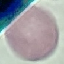
Summary:
  - Malaria status: uninfected
  - Image type: automatically extracted cell patch, resized to 64 × 64 pixels
  - Stain: Giemsa
  - Preparation: thin blood film
  - Capture: smartphone through the microscope eyepiece